Draw a bounding box around every Plasmodium parasite.
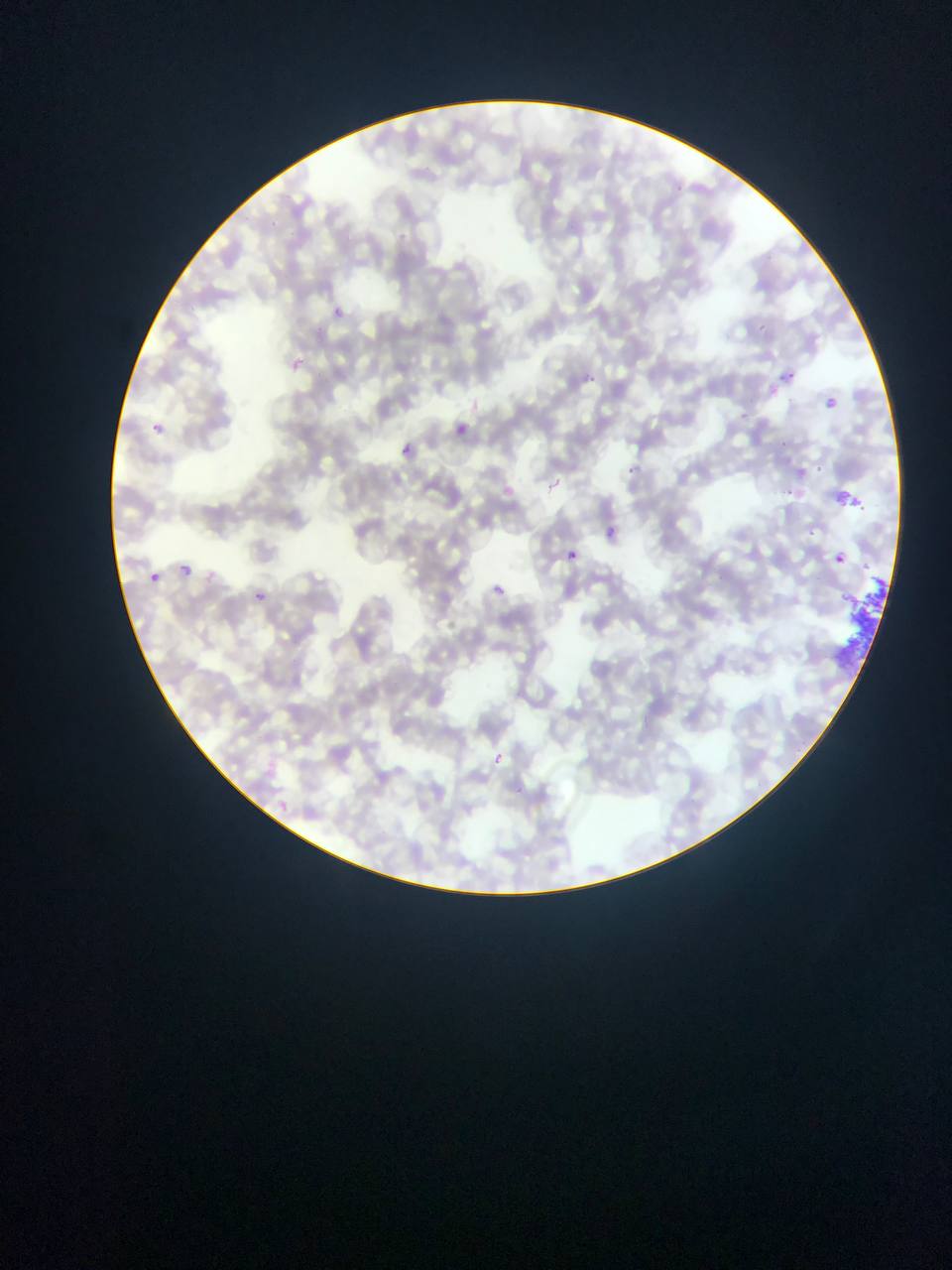

Approximate bounding boxes as [left, top, right, bottom] in pixels.
Plasmodium parasites: [332, 304, 345, 315], [753, 323, 769, 331], [288, 359, 310, 372], [788, 369, 796, 381], [587, 370, 599, 380], [739, 410, 748, 420], [150, 420, 163, 434], [401, 442, 415, 457], [812, 464, 825, 474], [626, 466, 636, 477], [785, 486, 796, 496], [566, 549, 578, 561], [833, 555, 847, 563], [181, 564, 193, 576], [491, 581, 511, 595], [254, 587, 266, 603], [491, 750, 510, 763].

image size = 952×1270 pixels
artifact (stain precipitate or debris) locations = approximate bounding boxes as [left, top, right, bottom] in pixels: [830, 571, 895, 672]
country = Ghana
preparation = thin blood smear
capture = mobile-phone photograph through a microscope
field of view = single